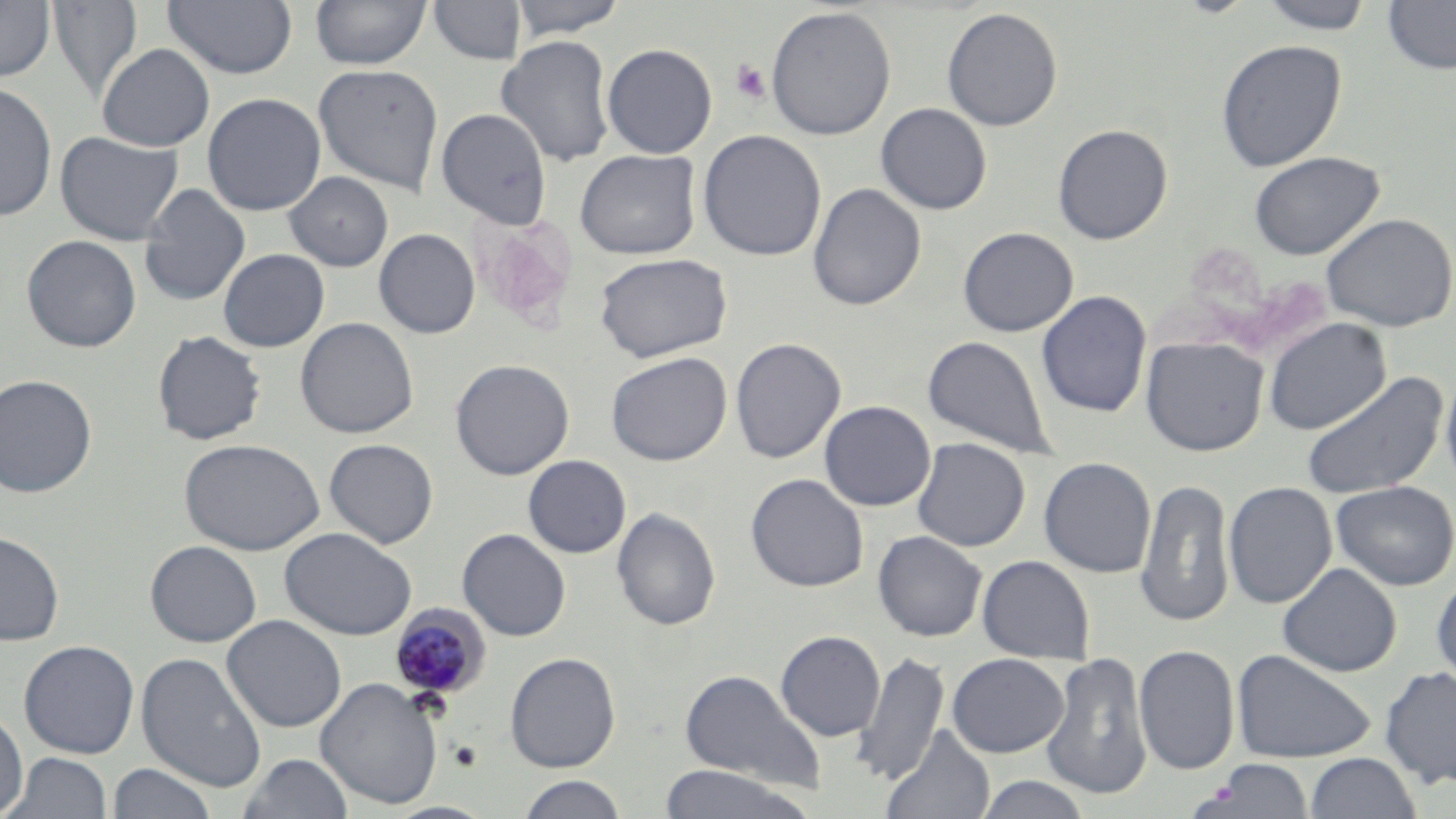
slide-level diagnosis = Plasmodium malariae
preparation = thin blood film
Plasmodium malariae-infected red blood cell locations = approximate bounding boxes as [x1, y1, x2, y2] in pixels: [389, 603, 491, 702]
magnification = 1000x
field of view = one of a larger specimen
modality = light microscopy
uninfected red blood cell locations = approximate bounding boxes as [x1, y1, x2, y2] in pixels: [162, 0, 298, 79], [310, 0, 432, 69], [509, 0, 628, 39], [1257, 0, 1376, 34], [0, 1, 56, 82], [48, 1, 143, 102], [427, 1, 526, 65], [1383, 1, 1456, 75], [765, 5, 897, 140], [941, 7, 1063, 131], [496, 35, 615, 167], [1215, 39, 1347, 172], [97, 43, 215, 151], [602, 43, 717, 158], [313, 62, 444, 196], [0, 81, 58, 222], [202, 92, 326, 216], [875, 103, 992, 214], [436, 107, 552, 228], [1052, 124, 1173, 244], [55, 130, 183, 246], [697, 130, 826, 261], [575, 149, 700, 260], [1249, 151, 1384, 260], [284, 171, 393, 271], [139, 184, 251, 305], [808, 184, 926, 310], [1320, 212, 1456, 332], [958, 226, 1078, 337], [374, 228, 480, 339], [21, 235, 141, 353], [218, 248, 329, 352], [594, 252, 733, 363], [1037, 290, 1151, 417], [295, 317, 419, 439], [1263, 317, 1391, 435], [152, 331, 267, 445], [922, 334, 1056, 460], [1140, 335, 1269, 456], [730, 337, 846, 463], [606, 351, 732, 466], [450, 358, 574, 480], [1440, 369, 1456, 497], [1301, 370, 1449, 500], [0, 374, 97, 497], [820, 400, 935, 511], [912, 437, 1030, 552], [179, 438, 324, 555], [324, 438, 438, 549], [523, 455, 631, 558], [1038, 457, 1156, 578], [745, 474, 868, 592], [1134, 478, 1235, 627], [1223, 481, 1337, 609], [1331, 481, 1456, 590], [612, 508, 721, 631], [279, 527, 417, 640], [457, 529, 571, 641], [0, 530, 64, 646], [872, 530, 987, 642], [145, 540, 262, 647], [977, 555, 1094, 663], [1278, 563, 1402, 677], [1431, 573, 1456, 689], [221, 615, 346, 733], [775, 630, 885, 741], [18, 639, 140, 759], [1134, 644, 1240, 775], [1232, 648, 1377, 763], [853, 649, 949, 787], [1041, 651, 1153, 800], [136, 652, 267, 792], [504, 652, 621, 772], [946, 653, 1068, 758], [1379, 666, 1456, 788], [679, 669, 827, 792], [315, 677, 443, 809], [0, 710, 28, 816], [881, 725, 996, 819], [6, 752, 112, 818], [238, 752, 355, 819], [1304, 752, 1422, 818], [1205, 761, 1315, 817], [106, 763, 218, 819], [659, 764, 814, 819], [516, 775, 630, 818], [974, 775, 1091, 819], [383, 801, 499, 819]
platelet locations = approximate bounding boxes as [x1, y1, x2, y2] in pixels: [731, 60, 770, 104]
stain = May-Grünwald-Giemsa
image size = 1456×819 pixels